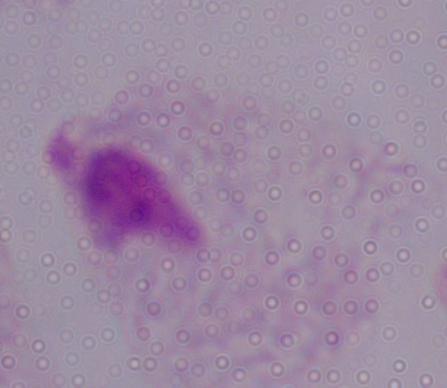
identification = trichomonad
modality = micrograph
magnification = 1000x